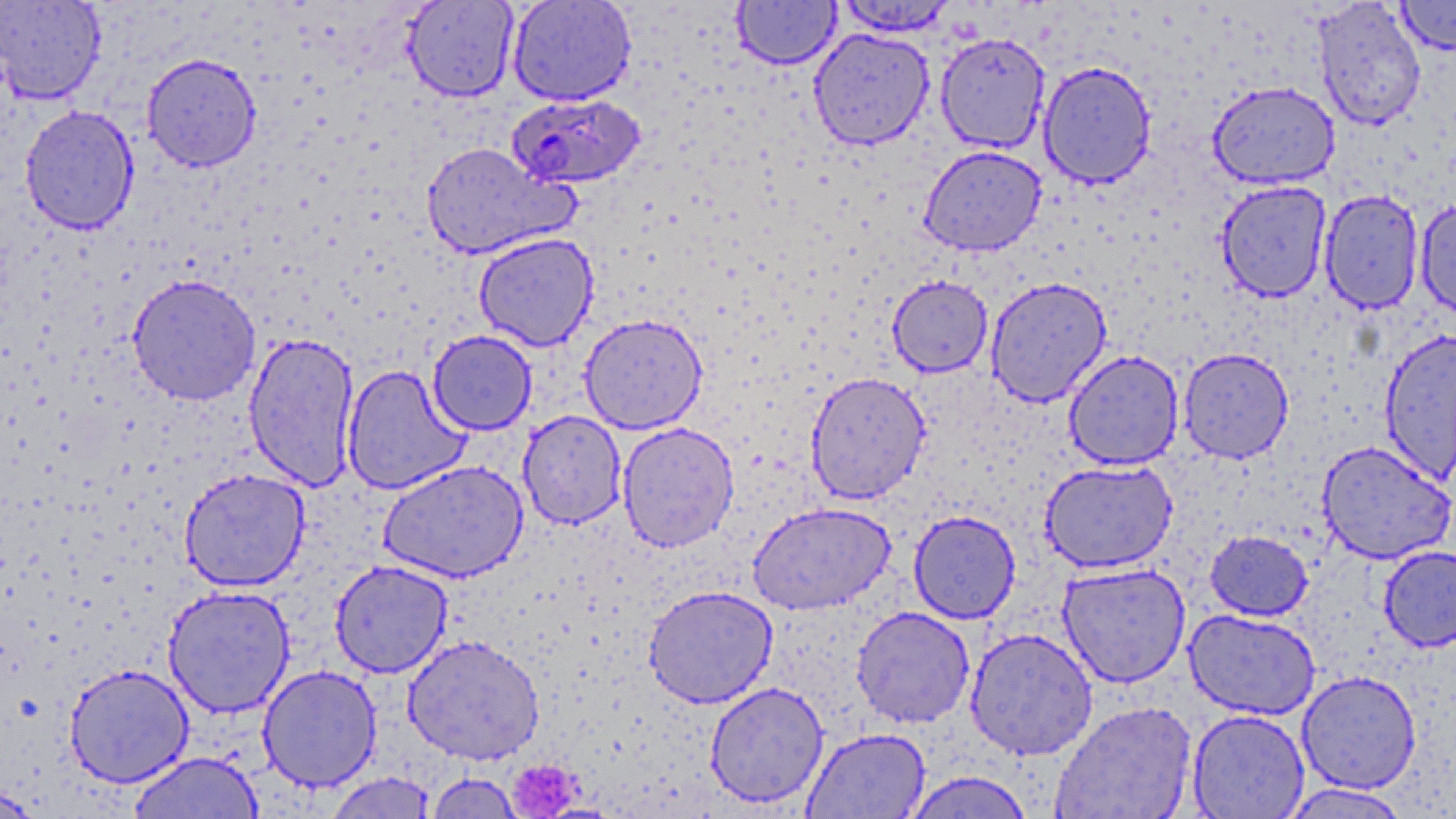
Approximate bounding boxes as [x1, y1, x2, y2] in pixels. Platelet locations: [507, 762, 589, 814]. Uninfected red blood cell locations: [0, 0, 106, 105], [507, 0, 636, 106], [1394, 0, 1456, 56], [402, 1, 519, 102], [732, 1, 841, 70], [834, 1, 960, 36], [1312, 1, 1427, 131], [808, 27, 934, 150], [935, 31, 1051, 154], [141, 53, 262, 172], [1038, 61, 1158, 189], [1208, 81, 1340, 190], [19, 105, 140, 235], [420, 141, 579, 260], [918, 145, 1047, 256], [1215, 180, 1332, 303], [1319, 189, 1424, 314], [1415, 199, 1456, 320], [473, 232, 599, 351], [126, 274, 262, 406], [887, 275, 993, 377], [985, 276, 1112, 408], [579, 313, 708, 434], [1379, 328, 1456, 484], [427, 330, 538, 435], [243, 332, 360, 491], [1177, 347, 1294, 464], [1063, 350, 1185, 471], [341, 364, 470, 495], [805, 371, 931, 505], [518, 410, 627, 530], [616, 422, 740, 552], [1316, 440, 1455, 565], [378, 460, 528, 583], [1039, 460, 1178, 574], [179, 468, 310, 592], [746, 501, 895, 615], [908, 510, 1021, 624], [1204, 530, 1314, 621], [1377, 545, 1456, 652], [330, 560, 454, 679], [1057, 562, 1192, 688], [162, 585, 295, 718], [643, 585, 778, 709], [851, 606, 976, 728], [1184, 609, 1321, 720], [965, 628, 1098, 760], [402, 634, 545, 764], [64, 663, 194, 788], [257, 665, 382, 792], [1297, 670, 1422, 794], [705, 682, 830, 809], [1050, 701, 1197, 819], [1187, 709, 1310, 819], [801, 728, 930, 818], [129, 751, 264, 819], [901, 771, 1037, 818], [323, 772, 437, 819], [425, 773, 525, 818], [0, 781, 45, 818], [1279, 783, 1412, 818]. Plasmodium falciparum-infected red blood cell locations: [506, 92, 647, 189]. Slide-level diagnosis: Plasmodium falciparum. Optical microscopy. Captured at 1000x magnification. Single field of view. May-Grünwald-Giemsa-stained preparation. Thin blood film. Image is 1456×819 pixels.